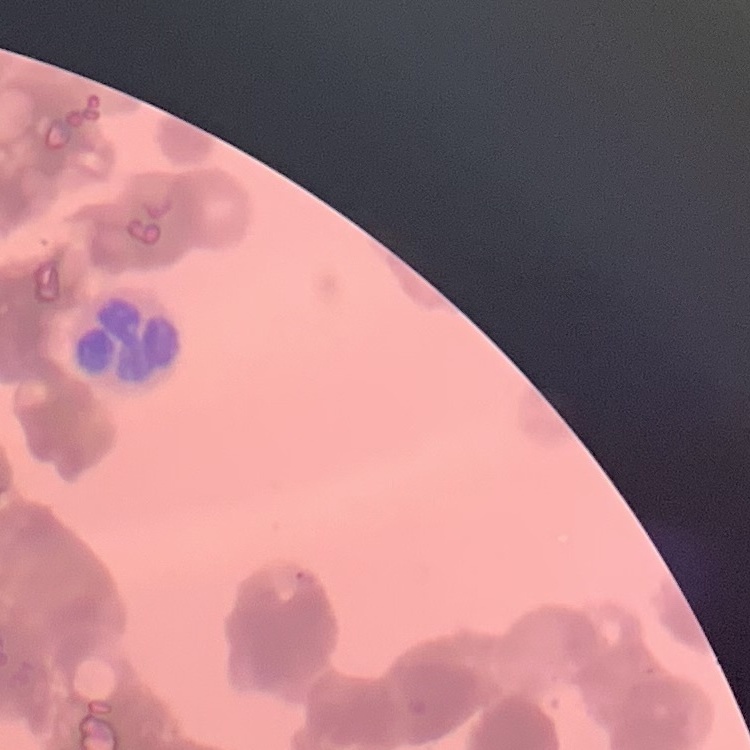
Summary:
  - Erythrocyte morphology: rouleaux formation
  - Preparation: thin blood smear
  - Image type: one tile cut from a larger photomicrograph
  - Stain: Field's or Giemsa